Give a bounding box for every artifact (stain precipitate or debris).
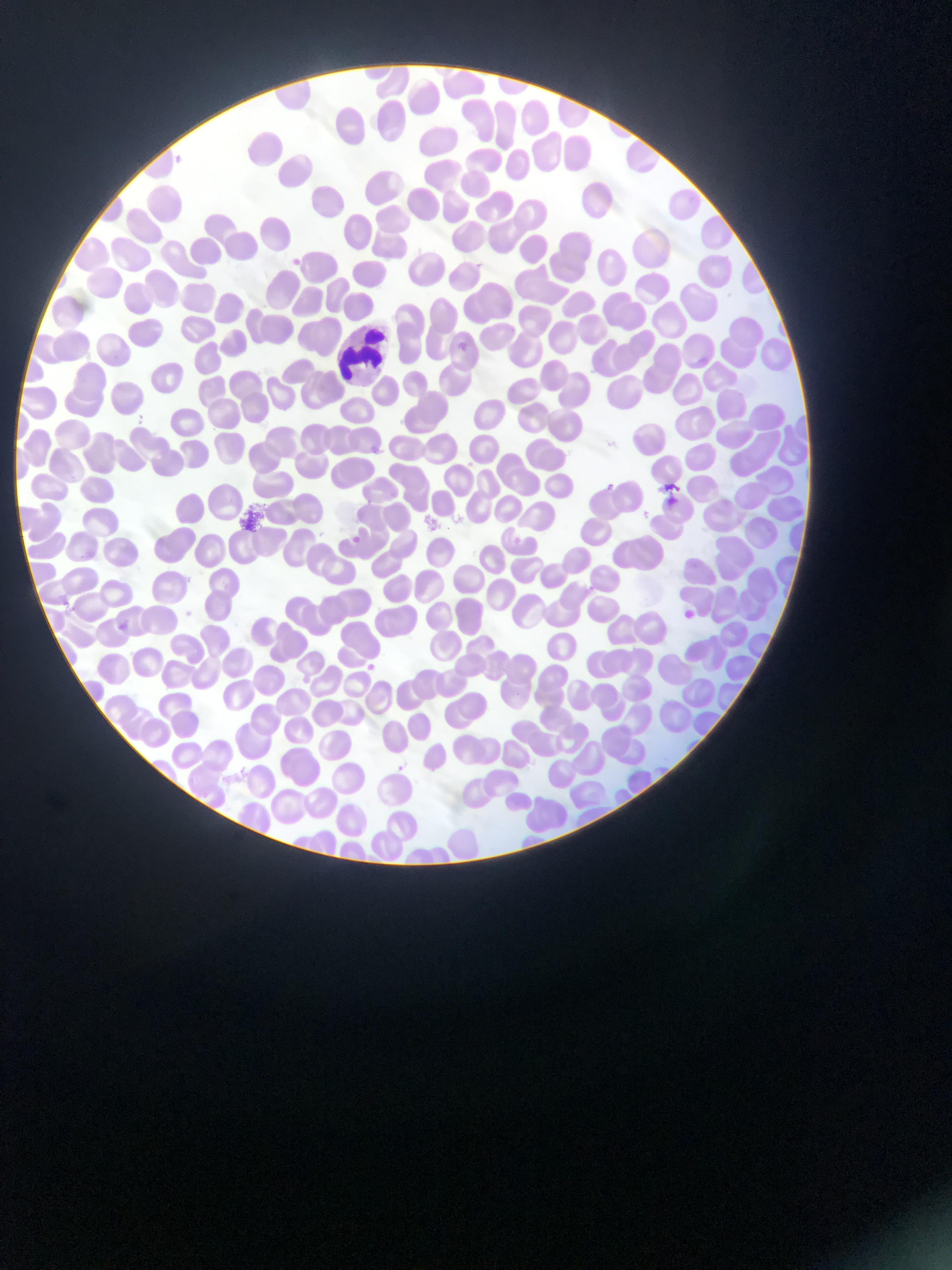
Approximate bounding boxes as [left, top, right, bottom] in pixels.
Artifacts (stain precipitate or debris): [234, 501, 275, 534].

Summary:
  - Plasmodium parasite locations: [452, 339, 470, 355], [598, 479, 624, 499], [603, 479, 618, 493], [638, 509, 651, 520], [348, 529, 370, 547], [349, 533, 363, 546], [509, 534, 522, 547], [57, 596, 72, 611], [179, 607, 196, 622], [681, 608, 696, 621], [114, 620, 129, 634], [364, 660, 379, 674]
  - Leukocyte locations: [335, 302, 400, 368]
  - Field of view: single
  - Capture: mobile-phone photograph through a microscope
  - Image size: 952×1270 pixels
  - Country: Ghana
  - Preparation: thin blood smear